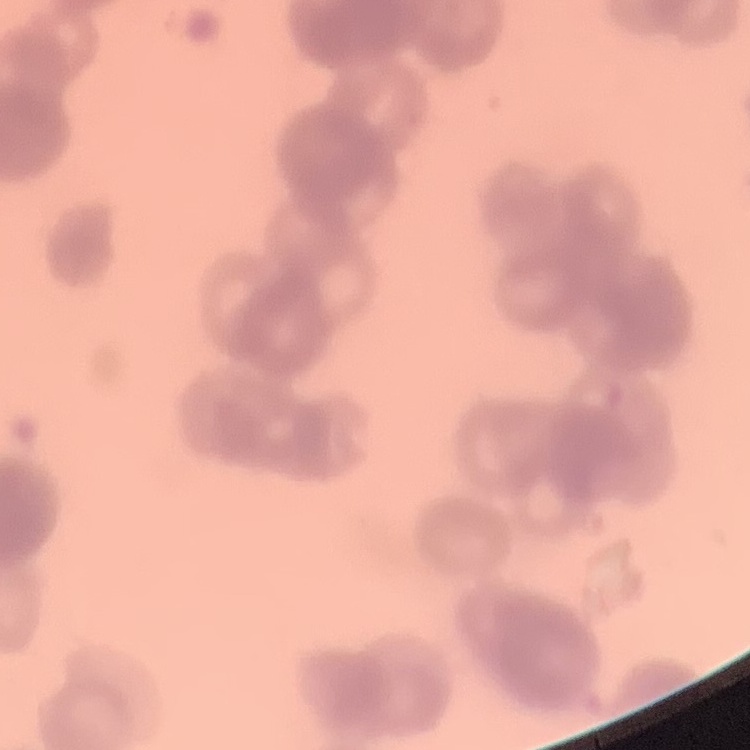

red_blood_cell_morphology: rouleaux formation
image_type: one tile cut from a larger photomicrograph
preparation: thin peripheral smear
stain: Field's or Giemsa